Identify the cell.
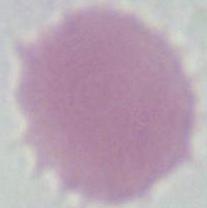

An erythrocyte.

1000x magnification. Micrograph.